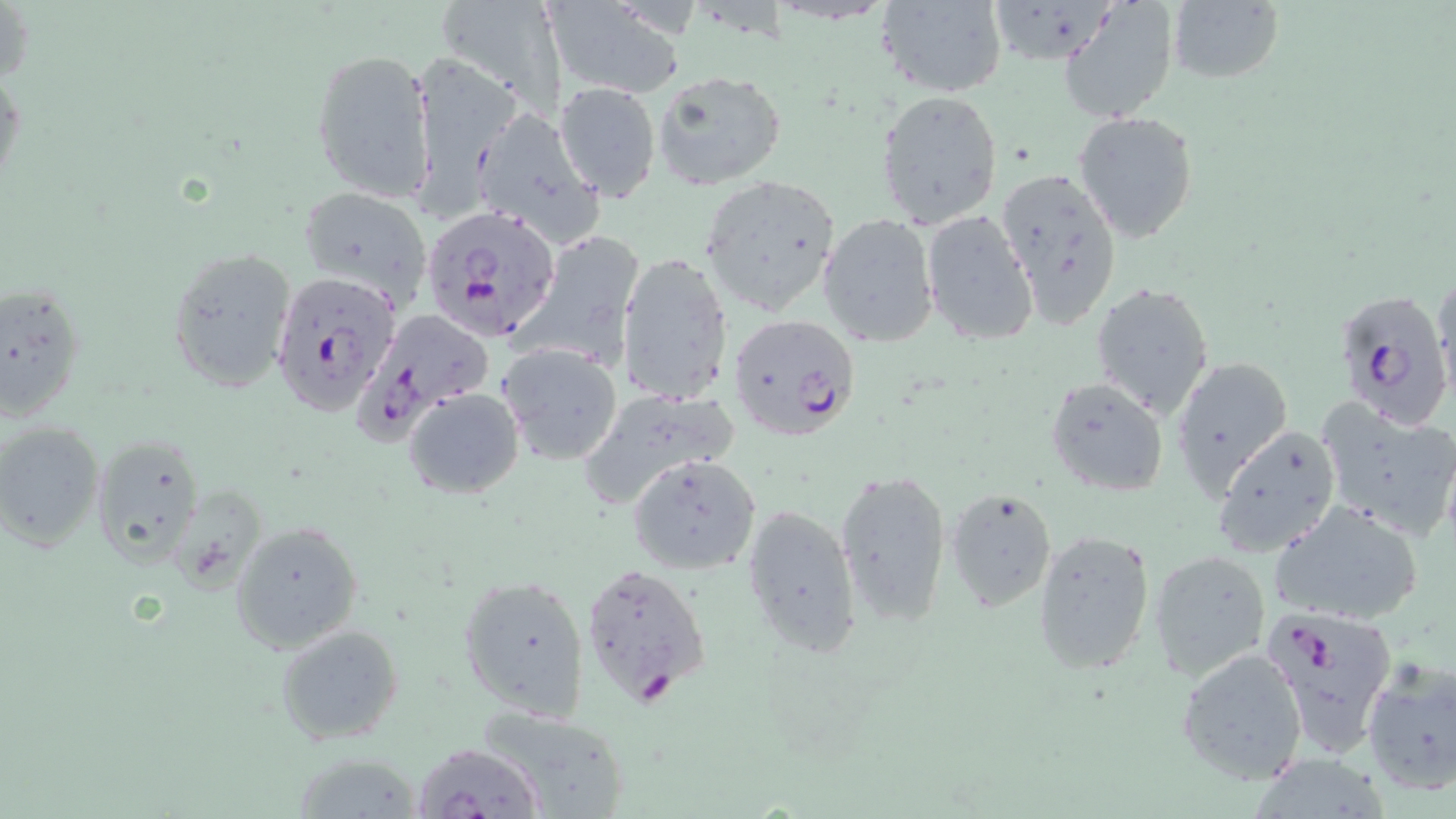
Summary:
  - Coordinate format: approximate bounding boxes as (x1,y1)-(x2,y2) corner pairs in pixels
  - Uninfected red blood cell locations: (433,0)-(565,114), (875,0)-(1007,98), (539,1)-(683,97), (985,1)-(1118,63), (1059,2)-(1179,124), (1166,2)-(1284,85), (310,48)-(434,203), (0,54)-(24,205), (413,61)-(515,224), (650,68)-(786,189), (553,81)-(662,202), (874,89)-(1004,230), (469,106)-(605,246), (1072,110)-(1199,243), (996,166)-(1125,330), (698,174)-(844,317), (297,186)-(434,308), (920,211)-(1039,346), (818,213)-(940,347), (518,229)-(645,365), (167,247)-(296,388), (617,251)-(735,408), (1432,271)-(1454,402), (1090,281)-(1216,420), (1,282)-(86,422), (498,343)-(622,464), (1167,356)-(1293,497), (1044,377)-(1170,497), (404,388)-(524,498), (576,389)-(739,509), (1317,396)-(1456,542), (0,421)-(105,552), (1211,424)-(1342,559), (89,430)-(208,566), (629,452)-(761,574), (834,468)-(954,630), (944,486)-(1059,613), (1270,500)-(1427,627), (742,501)-(863,658), (230,520)-(365,654), (1031,528)-(1157,676), (1149,548)-(1271,680), (458,574)-(590,720), (275,624)-(404,746), (1176,646)-(1310,785), (1359,657)-(1456,797), (475,704)-(632,818), (289,752)-(423,818), (1245,755)-(1395,817)
  - Plasmodium falciparum-infected red blood cell locations: (423,206)-(559,341), (271,271)-(404,416), (1331,287)-(1452,428), (359,307)-(497,438), (726,313)-(862,442), (578,561)-(711,708), (1264,601)-(1399,752), (409,741)-(543,818)
  - Slide-level diagnosis: Plasmodium falciparum
  - Preparation: thin blood film
  - Modality: optical microscopy
  - Stain: May-Grünwald-Giemsa
  - Magnification: 1000x
  - Image size: 1456×819 pixels
  - Field of view: one of a larger specimen